Assess for parasitized red blood cells.
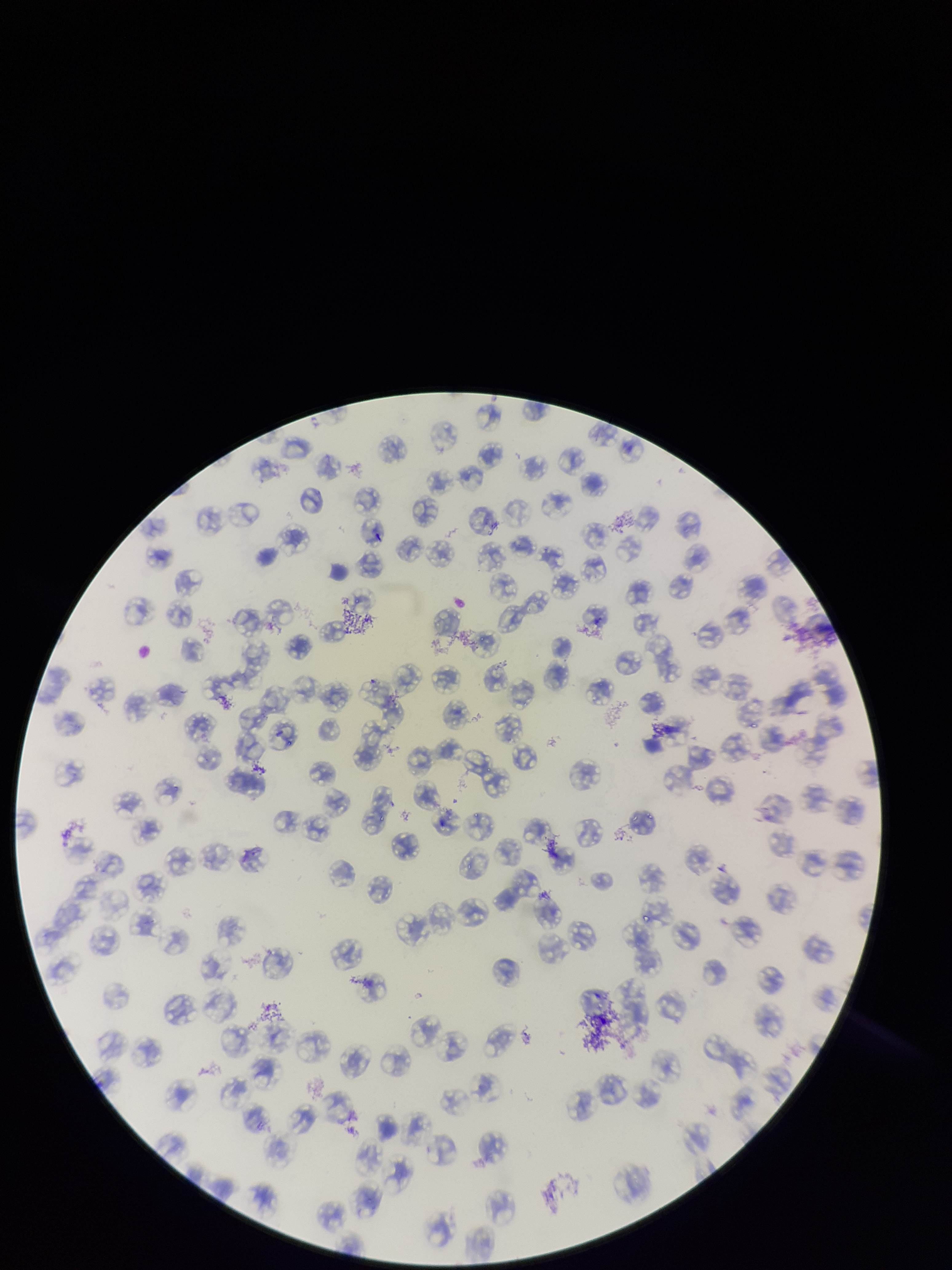
None detected.

Parasitized red blood cell count: 0. Smartphone photograph taken through the eyepiece of a microscope. Species reported for this patient: Plasmodium falciparum. Stained with Giemsa. Image is 952×1270 pixels. Red blood cell count: 131. Single field of view. Preparation: thin. Patient malaria status: positive.